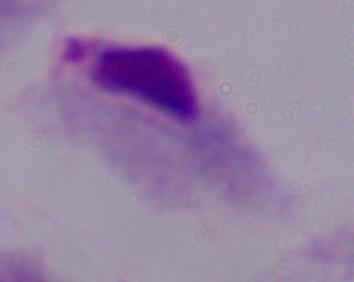

Summary:
  - Identification: trichomonad
  - Modality: photomicrograph
  - Magnification: 1000x